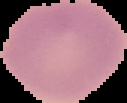
Summary:
  - Image size: 127×103 pixels
  - Result: no Plasmodium parasites detected
  - Image type: segmented cell region with the area outside set to black
  - Preparation: thin blood film